Identify the blood parasite species.
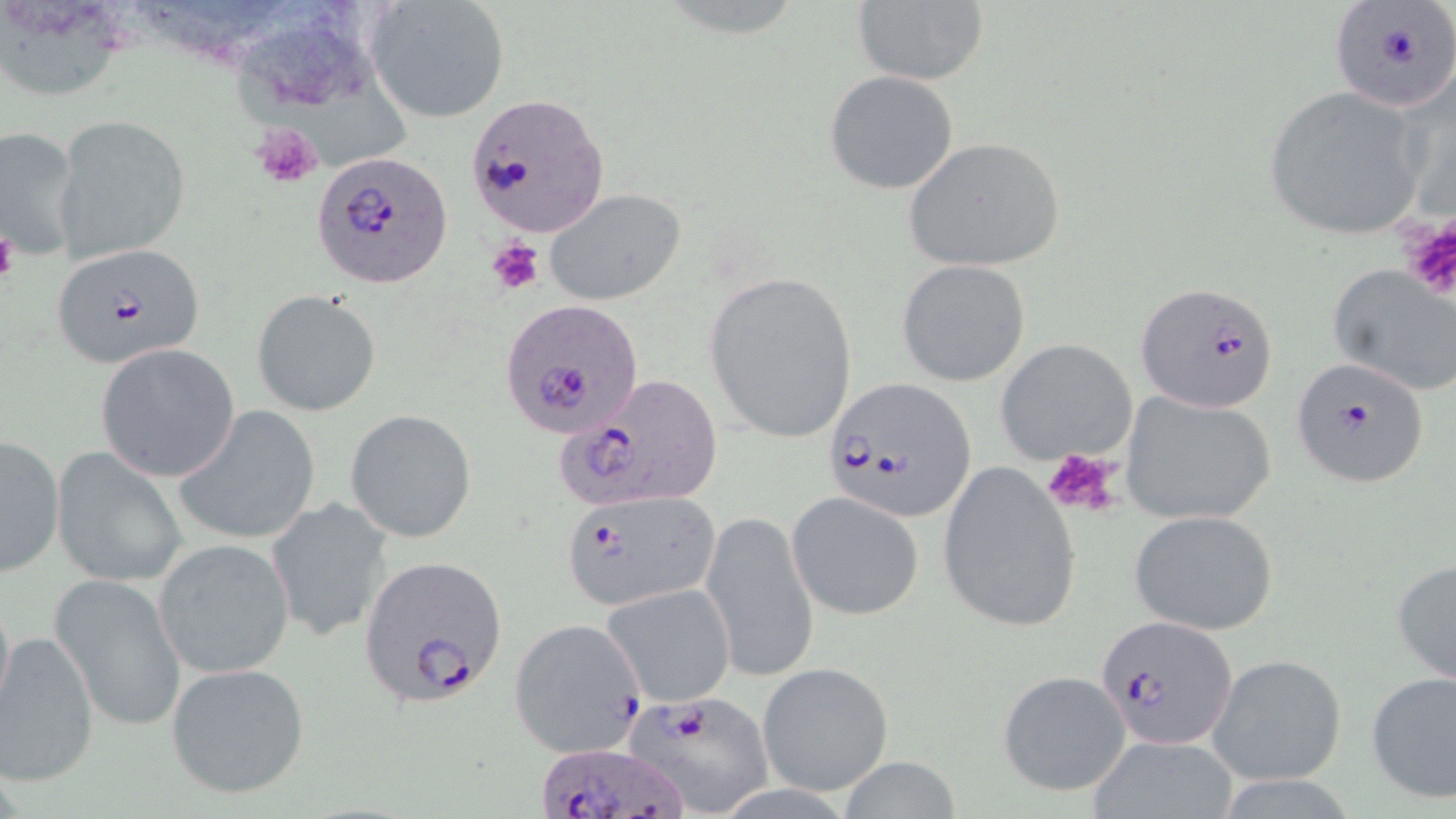

Plasmodium falciparum.

Approximate bounding boxes as (x1,y1)-(x2,y2) corner pairs in pixels. Uninfected red blood cell locations: (366,1)-(512,125), (849,2)-(989,87), (0,4)-(137,103), (133,4)-(291,60), (247,40)-(414,170), (824,71)-(959,195), (1261,85)-(1432,240), (53,114)-(192,266), (0,124)-(82,261), (902,136)-(1068,272), (543,188)-(687,306), (896,259)-(1031,387), (1325,262)-(1455,396), (704,270)-(857,441), (251,289)-(381,417), (995,338)-(1138,466), (95,342)-(241,483), (1119,391)-(1278,528), (174,405)-(320,546), (345,409)-(477,543), (1,434)-(66,577), (50,447)-(187,589), (937,460)-(1083,634), (787,491)-(924,620), (263,496)-(394,643), (700,506)-(819,685), (1128,509)-(1280,634), (153,538)-(296,679), (1391,555)-(1456,689), (50,575)-(186,733), (603,583)-(735,706), (0,630)-(100,788), (1206,652)-(1348,786), (166,661)-(313,801), (757,661)-(895,798), (996,670)-(1130,796), (1364,670)-(1456,805), (1086,734)-(1241,819), (833,757)-(968,818). Platelet locations: (250,123)-(324,191), (1396,216)-(1455,300), (0,226)-(19,289), (485,237)-(546,296), (1043,448)-(1124,517). Plasmodium falciparum-infected red blood cell locations: (1328,3)-(1454,115), (463,92)-(607,237), (315,152)-(452,288), (50,241)-(206,367), (1137,281)-(1280,414), (501,299)-(646,439), (1289,357)-(1432,489), (564,373)-(725,511), (822,379)-(977,522), (561,488)-(721,610), (360,556)-(509,707), (1097,613)-(1236,747), (507,617)-(647,758), (621,689)-(776,815), (535,740)-(683,819). One field of a larger specimen. Thin blood film. May-Grünwald-Giemsa-stained preparation. Optical microscopy. 1000x magnification. Image is 1456×819 pixels.